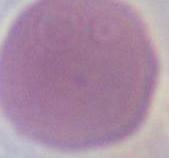
Captured at 1000x magnification. A red blood cell is seen. Photomicrograph.